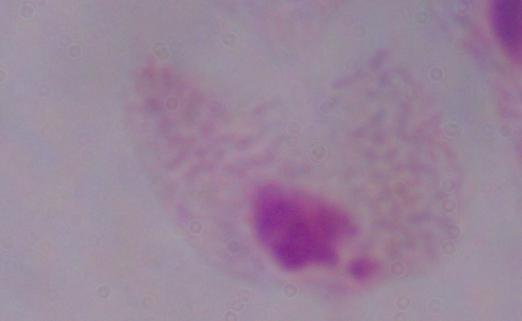

Micrograph. A trichomonad is shown. 1000x magnification.